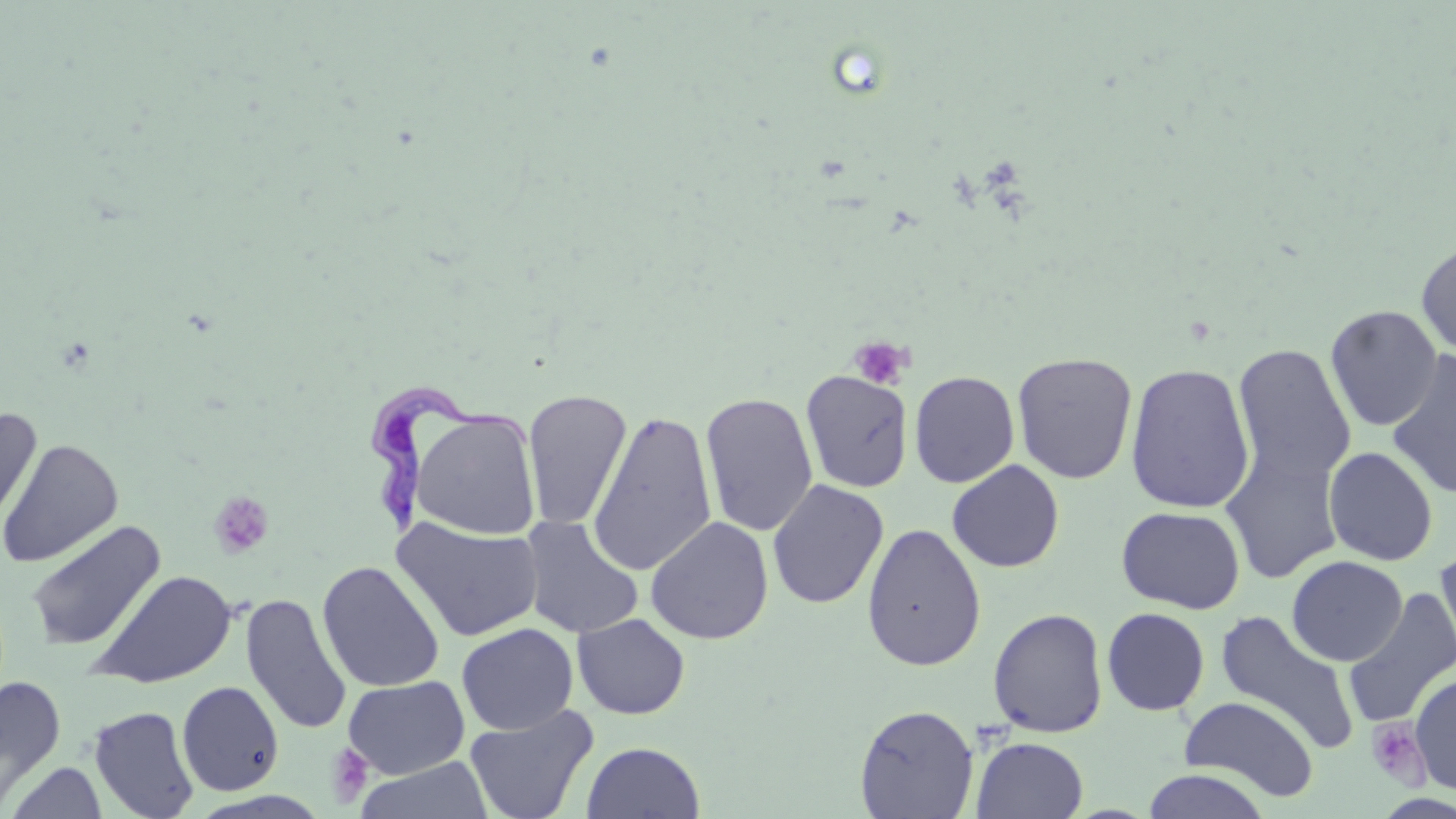

Summary:
  - Coordinate format: approximate bounding boxes as (x1, y1, x2, y2) in pixels
  - Trypanosoma brucei locations: (367, 387, 538, 540)
  - Platelet locations: (848, 335, 912, 391), (209, 491, 275, 559), (1366, 718, 1431, 789), (325, 743, 374, 807)
  - Uninfected red blood cell locations: (1416, 240, 1456, 359), (1325, 305, 1443, 431), (1232, 343, 1356, 487), (1386, 349, 1456, 500), (1012, 351, 1137, 485), (1124, 361, 1255, 514), (801, 369, 913, 493), (909, 370, 1020, 488), (523, 389, 632, 530), (700, 393, 818, 537), (0, 404, 41, 534), (410, 409, 541, 540), (588, 410, 718, 577), (0, 438, 124, 568), (1221, 443, 1344, 585), (1323, 447, 1438, 566), (947, 459, 1064, 573), (766, 478, 889, 609), (1117, 506, 1245, 613), (518, 515, 644, 639), (392, 516, 544, 642), (645, 516, 773, 645), (26, 520, 165, 651), (862, 522, 986, 672), (1435, 549, 1456, 670), (1286, 555, 1408, 667), (317, 561, 445, 693), (88, 569, 238, 689), (1343, 586, 1456, 729), (241, 593, 352, 735), (988, 607, 1109, 738), (1102, 608, 1210, 716), (1215, 609, 1359, 755), (572, 613, 690, 719), (456, 622, 578, 734), (1410, 671, 1456, 795), (343, 675, 470, 779), (0, 676, 66, 811), (177, 681, 284, 796), (1179, 696, 1319, 800), (854, 703, 979, 818), (464, 704, 599, 819), (90, 705, 200, 819), (972, 737, 1088, 819), (582, 742, 704, 818), (355, 756, 494, 818), (5, 762, 108, 818), (1141, 770, 1271, 818)
  - Slide-level diagnosis: Trypanosoma brucei
  - Modality: optical microscopy
  - Preparation: thin blood film
  - Field of view: one of a larger specimen
  - Magnification: 1000x
  - Stain: May-Grünwald-Giemsa
  - Image size: 1456×819 pixels